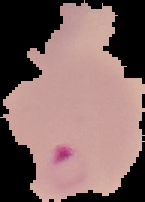

Malaria status: parasitized. Cell region segmented out of the field of view; the surrounding area is masked to black. Image is 145×202 pixels. From a thin blood smear.